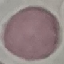
Malaria status: uninfected. Cell patch, automatically extracted from a larger field of view and resized to 64 × 64 pixels. Acquired by smartphone through the microscope eyepiece. Giemsa stain. Thin blood film.